Give the position of every Plasmodium parasite.
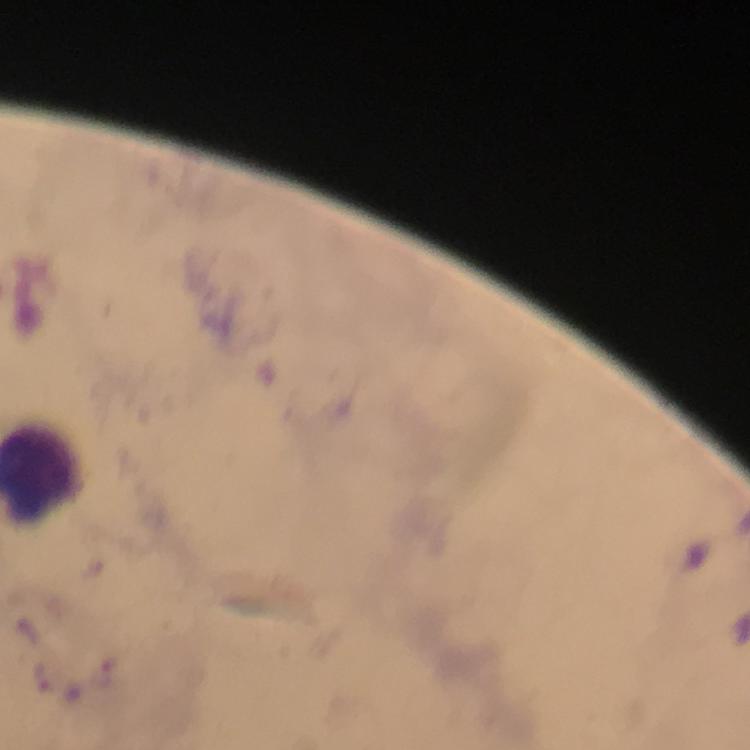

Approximate centers as (x, y) in pixels.
Plasmodium parasites: (103, 672), (43, 675).

Summary:
  - Preparation: thick blood film
  - Magnification: 100x
  - Immersion oil: applied
  - Stain: Giemsa
  - Cropped from: one field of view
  - Capture: smartphone photograph through a microscope
  - Context: from a malaria diagnostic workup
  - Image size: 750×750 pixels